Assess this cell for malaria.
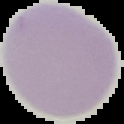
Uninfected.

Summary:
  - Image type: cell region segmented out of the field of view; surrounding area masked to black
  - Image size: 124×124 pixels
  - Preparation: thin blood smear